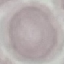

Summary:
  - Malaria status: uninfected
  - Capture: smartphone camera at the microscope eyepiece
  - Preparation: thin blood smear
  - Image type: automatically extracted cell patch, resized to 64 × 64 pixels
  - Stain: Giemsa